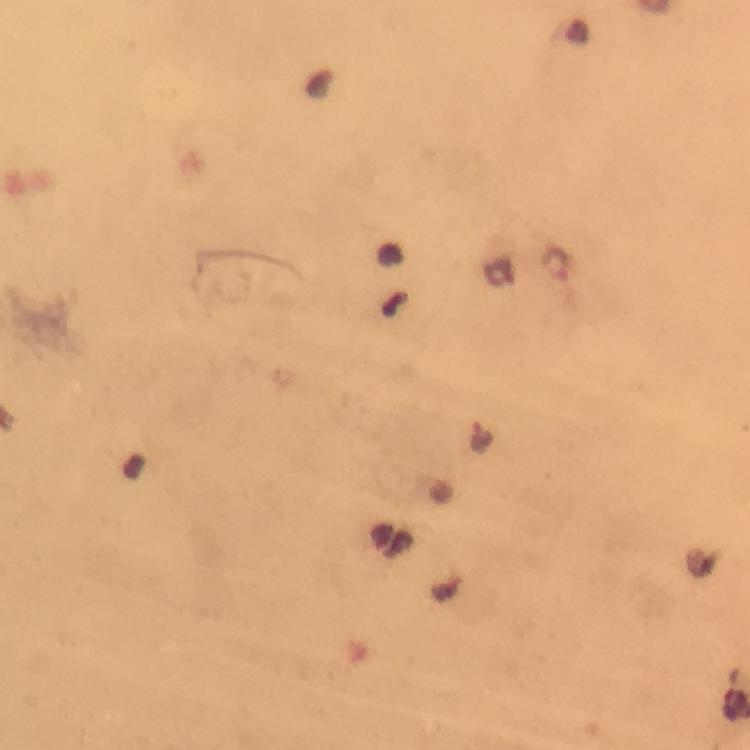
magnification = 100x
capture = smartphone mounted on the microscope
context = from a diagnostic examination for malaria
Plasmodium parasite locations = approximate centers as {x, y} in pixels: {555, 262}, {481, 436}
stain = Giemsa
image size = 750×750 pixels
preparation = thick blood film
immersion oil = applied
cropped from = a single field of view